Comment on the morphology of the red blood cells.
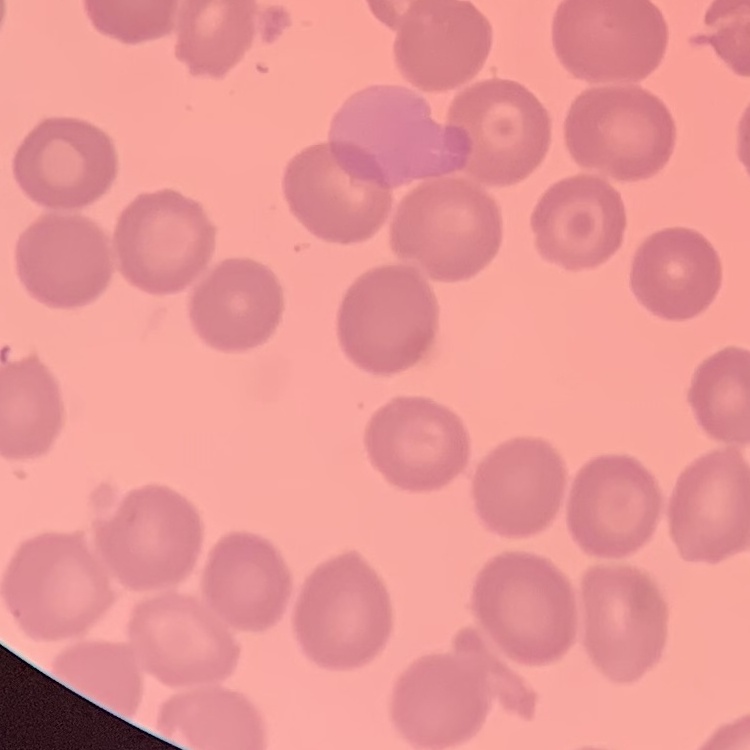
No rouleaux formation.

preparation = thin blood film
stain = Field's or Giemsa
image type = one tile cut from a larger photomicrograph